Classify this cell by malaria status.
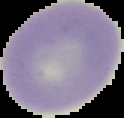
It is uninfected.

image_size: 124×118 pixels
image_type: segmented cell region with the area outside set to black
preparation: thin blood film